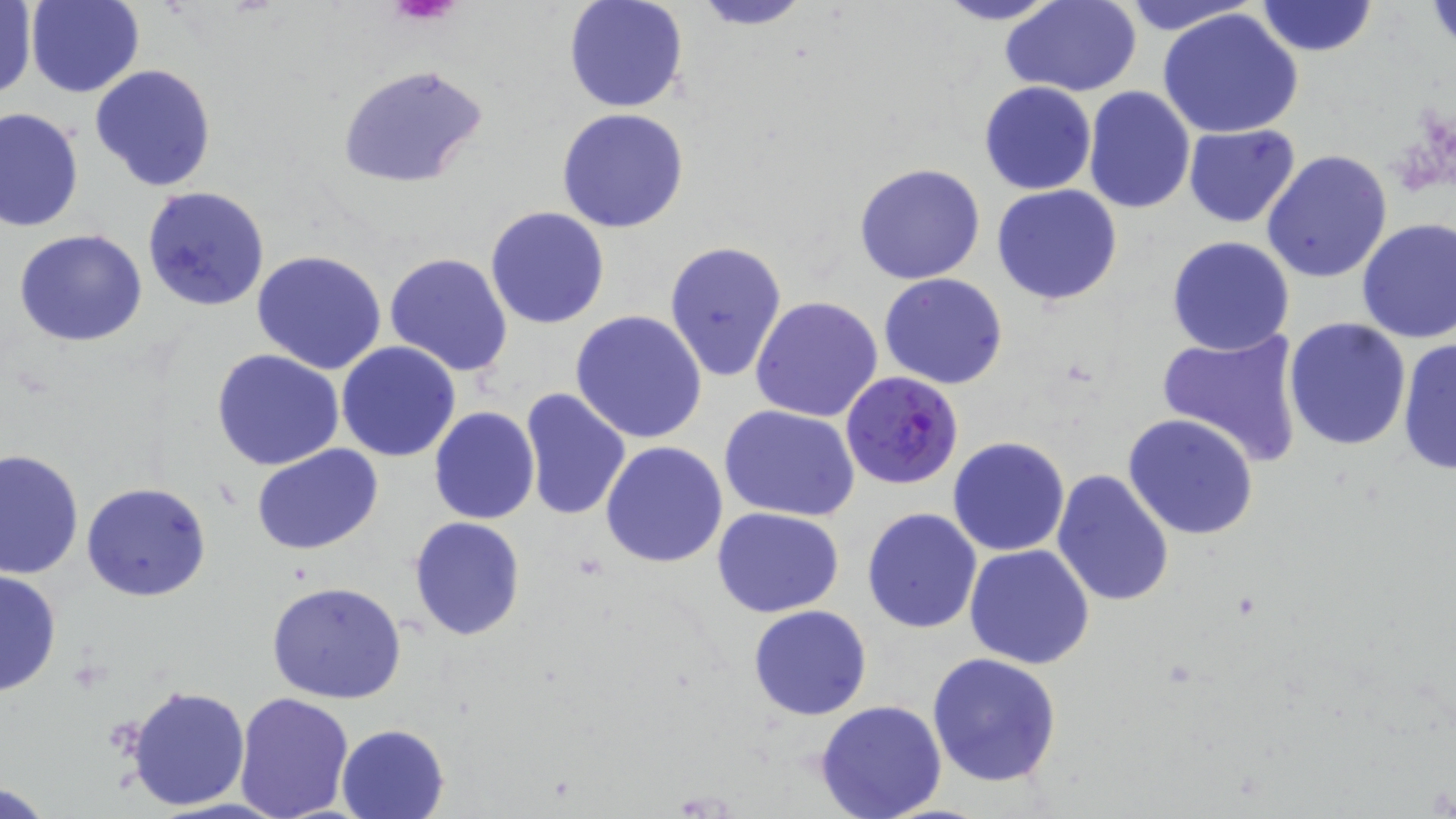

{
  "slide_level_diagnosis": "Plasmodium falciparum",
  "image_size": "1456×819 pixels",
  "modality": "light microscopy",
  "stain": "May-Grünwald-Giemsa",
  "field_of_view": "single",
  "magnification": "1000x",
  "plasmodium_falciparum_infected_red_blood_cell_locations": "approximate bounding boxes as [x1, y1, x2, y2] in pixels: [840, 373, 965, 489]",
  "preparation": "thin blood smear",
  "platelet_locations": "approximate bounding boxes as [x1, y1, x2, y2] in pixels: [387, 0, 466, 27]",
  "uninfected_red_blood_cell_locations": "approximate bounding boxes as [x1, y1, x2, y2] in pixels: [562, 0, 690, 115], [687, 0, 816, 30], [930, 0, 1066, 26], [1113, 0, 1266, 35], [1255, 0, 1377, 57], [26, 1, 143, 98], [1427, 1, 1456, 55], [1001, 2, 1142, 96], [1, 3, 37, 102], [1158, 8, 1305, 139], [335, 62, 487, 189], [89, 64, 219, 193], [979, 81, 1097, 196], [1082, 86, 1195, 213], [0, 106, 84, 231], [557, 108, 690, 233], [1183, 124, 1301, 228], [1261, 149, 1393, 285], [854, 162, 986, 284], [991, 184, 1123, 306], [141, 186, 271, 312], [485, 206, 611, 329], [1356, 218, 1455, 344], [14, 229, 148, 347], [1165, 235, 1294, 356], [662, 239, 786, 383], [251, 249, 387, 376], [385, 251, 514, 377], [878, 274, 1007, 390], [751, 295, 883, 424], [571, 310, 708, 444], [1283, 317, 1412, 451], [1155, 325, 1307, 469], [1397, 337, 1455, 474], [335, 341, 461, 462], [211, 349, 345, 471], [519, 387, 632, 521], [719, 405, 860, 523], [428, 407, 540, 526], [1124, 413, 1258, 541], [947, 436, 1071, 556], [601, 442, 729, 569], [252, 444, 384, 554], [0, 448, 83, 579], [1051, 469, 1176, 608], [82, 482, 212, 602], [713, 506, 843, 618], [861, 507, 982, 631], [409, 517, 527, 641], [964, 544, 1095, 667], [0, 569, 62, 698], [266, 580, 408, 703], [748, 604, 872, 720], [926, 653, 1063, 790], [123, 684, 251, 812], [233, 691, 355, 819], [814, 699, 948, 819], [336, 723, 450, 819], [1, 780, 57, 817]"
}